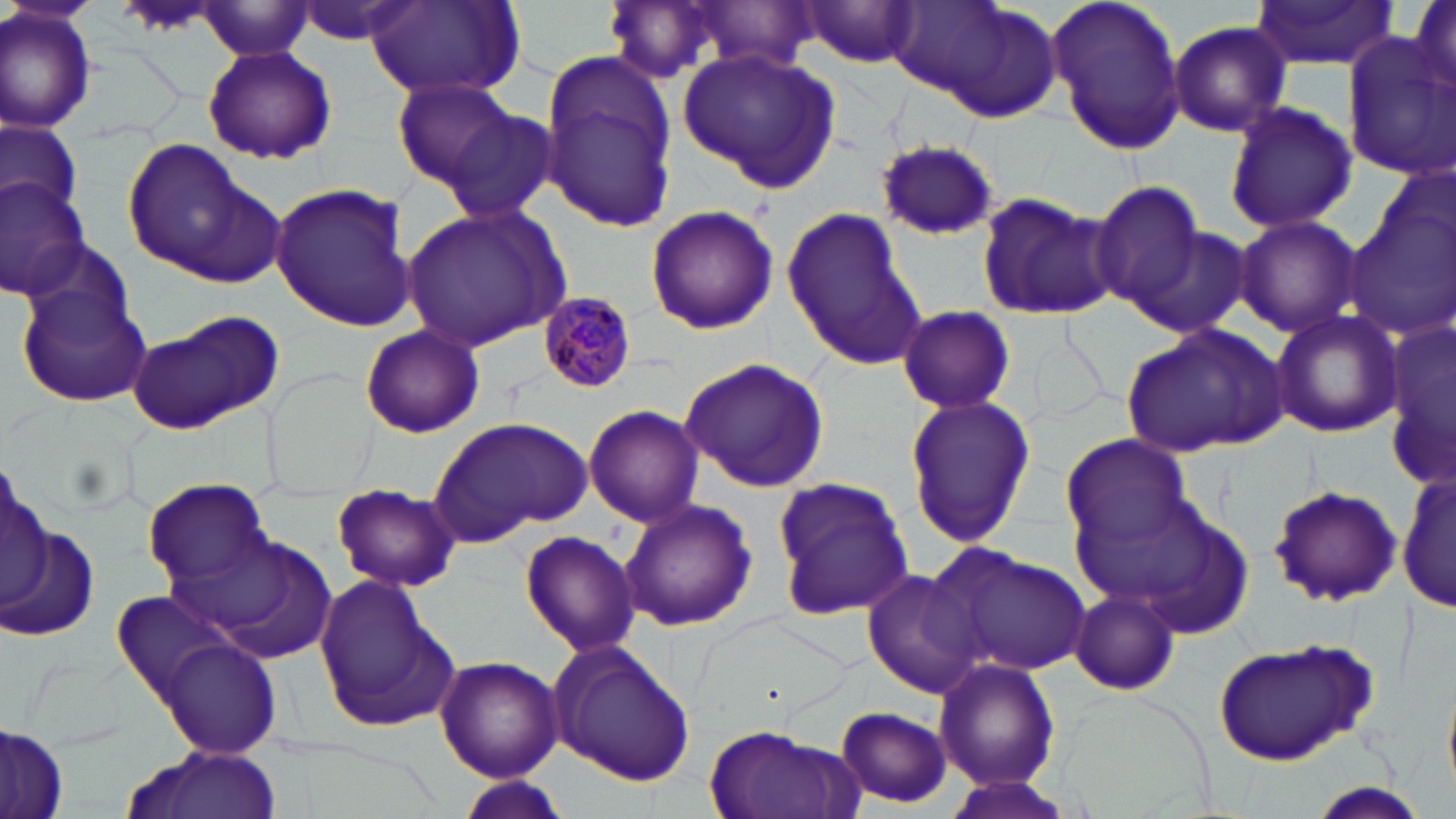
{
  "slide_level_diagnosis": "Plasmodium malariae",
  "image_size": "1456×819 pixels",
  "plasmodium_malariae_infected_red_blood_cell_locations": "approximate bounding boxes as [x1, y1, x2, y2] in pixels: [540, 294, 634, 394]",
  "modality": "light microscopy",
  "preparation": "thin blood smear",
  "magnification": "1000x",
  "stain": "May-Grünwald-Giemsa",
  "field_of_view": "one of a larger specimen",
  "uninfected_red_blood_cell_locations": "approximate bounding boxes as [x1, y1, x2, y2] in pixels: [799, 0, 921, 71], [885, 0, 1061, 118], [1048, 0, 1187, 156], [1408, 0, 1456, 93], [292, 1, 412, 46], [364, 1, 521, 102], [1249, 1, 1399, 69], [676, 2, 826, 75], [195, 4, 315, 60], [0, 5, 99, 134], [1168, 20, 1290, 137], [1342, 34, 1456, 181], [201, 45, 337, 165], [678, 47, 841, 193], [538, 49, 680, 233], [389, 75, 526, 196], [1223, 100, 1356, 234], [436, 101, 562, 225], [1, 118, 83, 220], [120, 138, 280, 281], [875, 140, 999, 241], [1360, 174, 1456, 331], [0, 176, 93, 298], [1088, 180, 1212, 317], [270, 182, 416, 331], [975, 190, 1118, 322], [403, 204, 566, 351], [645, 204, 778, 336], [782, 208, 924, 369], [1234, 215, 1361, 337], [1132, 227, 1251, 337], [17, 280, 152, 405], [897, 305, 1014, 413], [1270, 309, 1402, 439], [128, 312, 286, 434], [1385, 312, 1456, 492], [1123, 322, 1290, 458], [359, 324, 484, 439], [679, 357, 829, 492], [902, 393, 1036, 549], [583, 404, 703, 527], [434, 415, 593, 544], [1059, 433, 1196, 555], [1, 456, 48, 611], [1399, 463, 1452, 618], [140, 476, 272, 588], [771, 476, 916, 619], [331, 483, 462, 593], [1267, 483, 1405, 609], [1070, 486, 1255, 628], [619, 498, 758, 632], [3, 526, 99, 642], [185, 529, 339, 661], [517, 531, 641, 657], [930, 542, 1093, 679], [863, 569, 984, 699], [314, 577, 456, 732], [106, 585, 250, 717], [1070, 589, 1179, 694], [157, 636, 282, 759], [1212, 638, 1377, 766], [548, 641, 696, 788], [434, 654, 563, 784], [934, 657, 1060, 793], [836, 706, 953, 809], [702, 723, 861, 819], [0, 725, 67, 818], [122, 745, 282, 819], [940, 774, 1084, 819], [458, 778, 574, 818]"
}